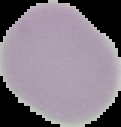
Summary:
  - Preparation: thin blood film
  - Image type: cell region segmented out of the field of view; surrounding area masked to black
  - Image size: 121×127 pixels
  - Malaria status: uninfected